Outline each Trypanosoma brucei.
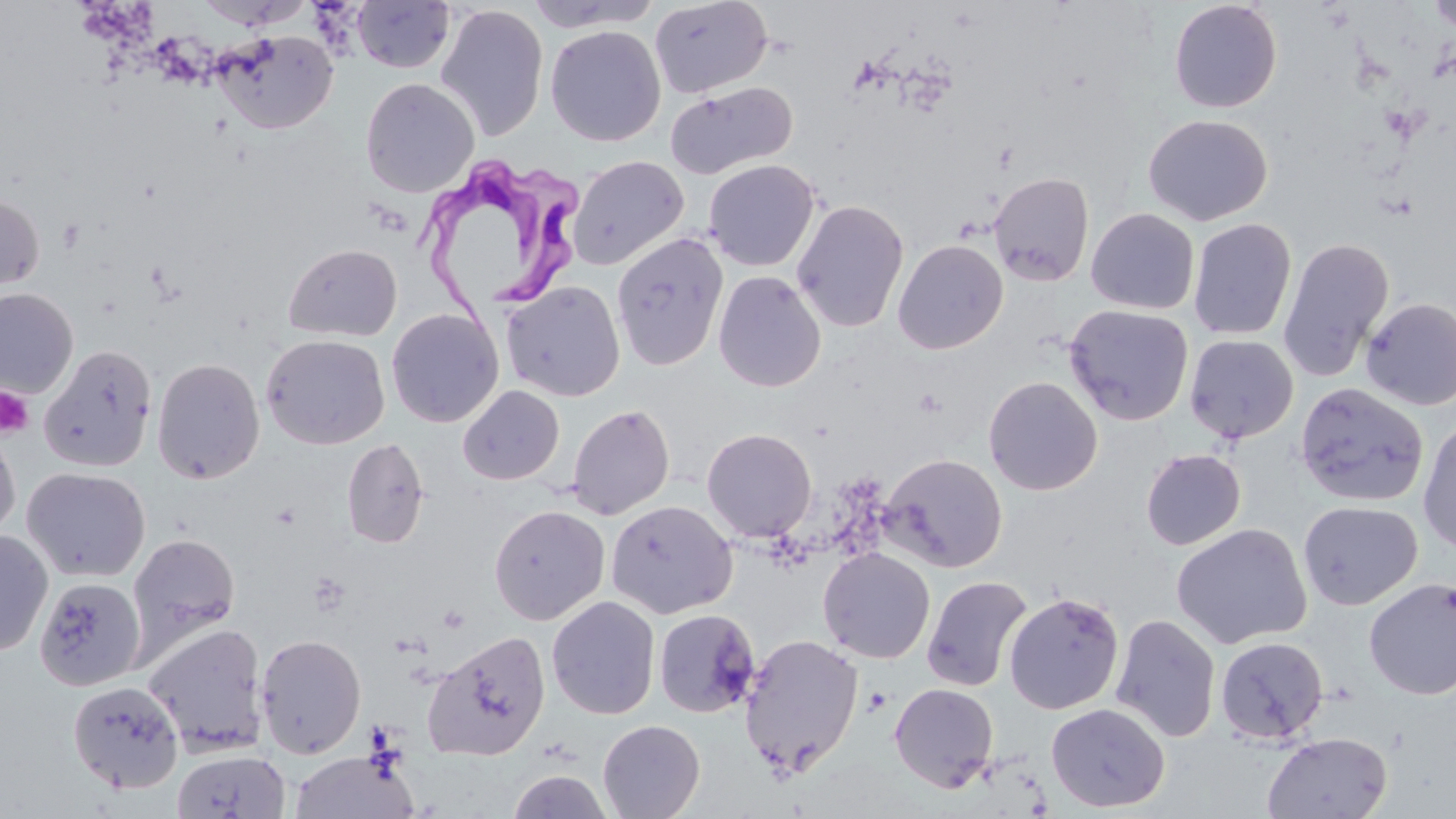

Approximate bounding boxes as [x1, y1, x2, y2] in pixels.
Trypanosoma brucei: [416, 154, 589, 317].

Uninfected red blood cell locations: [195, 0, 313, 29], [521, 0, 662, 32], [649, 0, 772, 98], [351, 1, 455, 74], [1168, 1, 1283, 113], [1427, 1, 1456, 35], [435, 5, 549, 142], [546, 25, 665, 146], [212, 29, 339, 135], [360, 78, 480, 198], [665, 81, 797, 179], [1143, 114, 1273, 225], [567, 155, 689, 270], [703, 159, 820, 271], [989, 172, 1095, 287], [0, 192, 44, 297], [791, 199, 909, 333], [1085, 207, 1200, 314], [1187, 218, 1297, 340], [789, 224, 1008, 344], [611, 233, 729, 370], [1278, 237, 1394, 381], [892, 239, 1008, 354], [283, 243, 402, 342], [713, 270, 826, 392], [500, 281, 625, 402], [1, 288, 78, 398], [1360, 297, 1456, 411], [1064, 304, 1194, 426], [386, 308, 504, 428], [261, 334, 390, 450], [1184, 334, 1299, 444], [38, 345, 157, 472], [151, 357, 265, 485], [983, 375, 1102, 495], [1296, 382, 1429, 507], [458, 384, 564, 485], [567, 403, 675, 519], [1418, 418, 1456, 555], [0, 425, 21, 543], [702, 427, 817, 542], [342, 437, 429, 548], [1140, 448, 1246, 550], [879, 453, 1008, 572], [21, 466, 151, 582], [605, 499, 738, 619], [1298, 500, 1422, 610], [488, 504, 610, 625], [1171, 523, 1312, 649], [0, 529, 53, 657], [128, 532, 240, 656], [818, 547, 936, 663], [922, 575, 1032, 691], [34, 576, 146, 690], [1363, 577, 1456, 699], [1003, 592, 1124, 714], [547, 596, 661, 720], [653, 609, 760, 718], [1110, 613, 1221, 742], [142, 621, 269, 756], [423, 631, 551, 761], [255, 633, 367, 759], [739, 634, 864, 775], [1215, 635, 1329, 746], [68, 681, 184, 793], [889, 682, 999, 792], [1046, 703, 1170, 812], [598, 718, 705, 819], [1261, 731, 1393, 819], [172, 749, 291, 819], [290, 749, 418, 819], [507, 769, 613, 819]. Platelet locations: [0, 386, 34, 438], [862, 686, 892, 717]. Slide-level diagnosis: Trypanosoma brucei. Image is 1456×819 pixels. Captured at 1000x magnification. Light microscopy. Single field of view. May-Grünwald-Giemsa-stained preparation. Thin blood film.